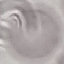
{
  "malaria_status": "uninfected",
  "capture": "smartphone through the microscope eyepiece",
  "stain": "Giemsa",
  "preparation": "thin blood smear",
  "image_type": "automatically extracted cell patch, resized to 64 × 64 pixels"
}